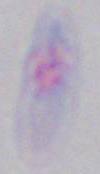
magnification = 1000x
identification = Toxoplasma gondii
modality = photomicrograph